Identify the parasite.
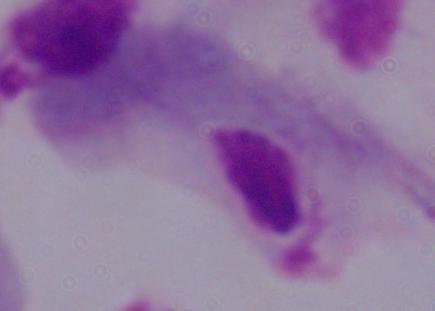
A trichomonad.

Summary:
  - Modality: photomicrograph
  - Magnification: 1000x